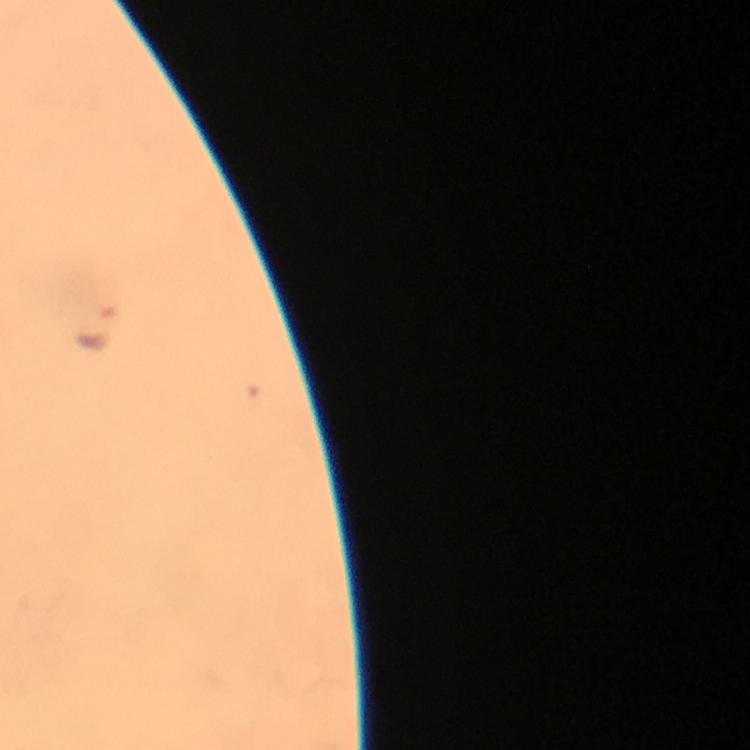
magnification = 100x
preparation = thick blood film
malaria parasite locations = approximate centers as {x, y} in pixels: {96, 329}
stain = Giemsa
immersion oil = applied
capture = smartphone mounted on the microscope
context = from a diagnostic examination for malaria
cropped from = a single field of view
image size = 750×750 pixels